Outline each uninfected red blood cell.
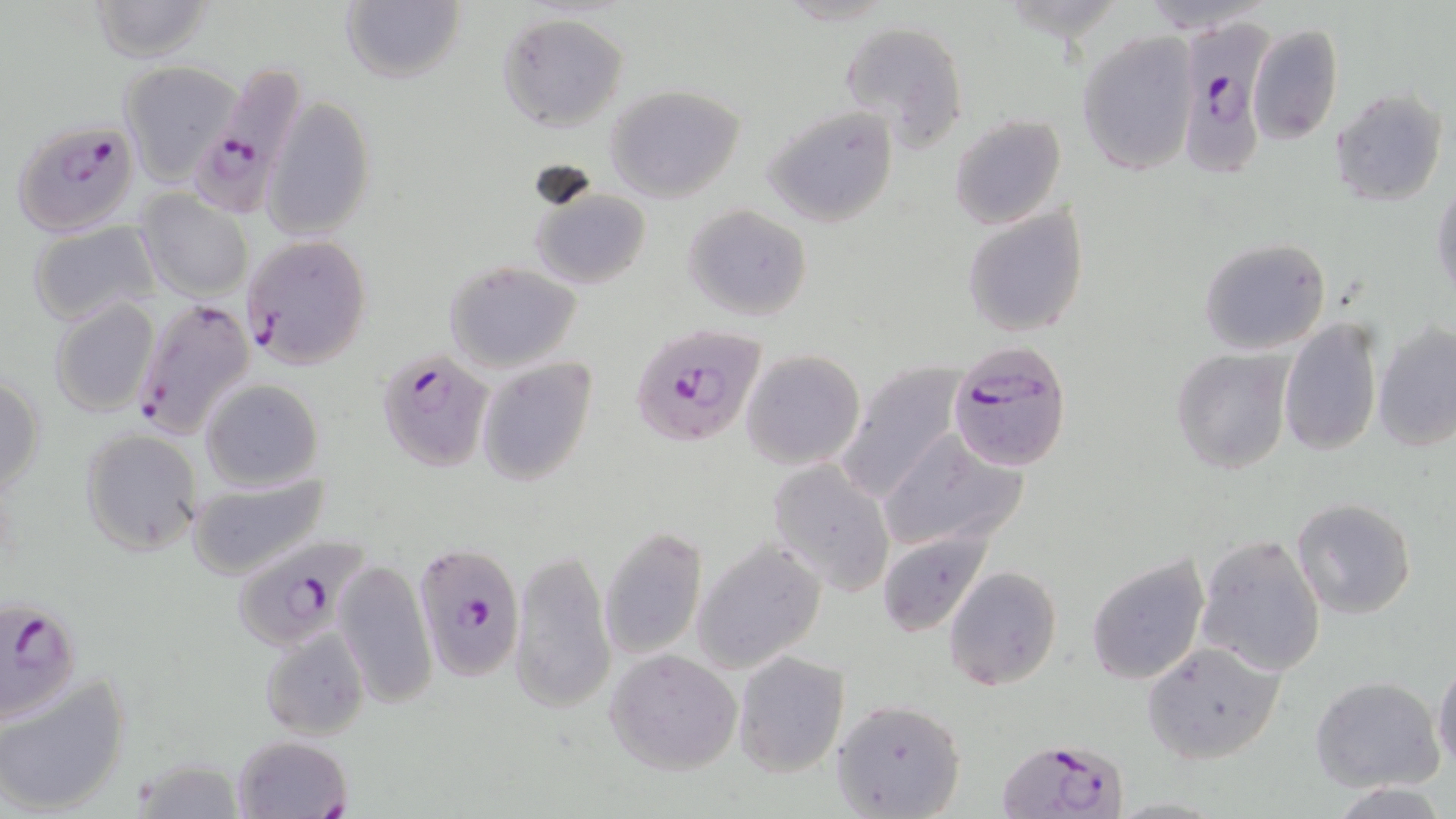
Approximate bounding boxes as (x1, y1, x2, y2) in pixels.
Uninfected red blood cells: (84, 0, 219, 63), (340, 0, 465, 86), (498, 12, 627, 131), (838, 19, 969, 152), (1249, 24, 1343, 144), (1076, 33, 1199, 174), (119, 62, 242, 186), (608, 85, 744, 202), (1331, 88, 1447, 207), (264, 99, 376, 239), (762, 105, 898, 227), (950, 114, 1066, 231), (1431, 175, 1456, 303), (530, 183, 651, 291), (134, 191, 253, 300), (682, 203, 813, 321), (962, 205, 1089, 338), (28, 222, 162, 329), (1198, 238, 1331, 356), (443, 258, 584, 373), (48, 298, 160, 419), (1277, 318, 1383, 458), (1373, 322, 1456, 453), (1171, 347, 1293, 475), (741, 348, 866, 470), (476, 357, 596, 487), (836, 359, 969, 507), (0, 374, 45, 495), (202, 379, 324, 489), (79, 428, 202, 554), (876, 431, 1029, 554), (768, 461, 896, 597), (185, 471, 335, 581), (1290, 497, 1418, 620), (599, 527, 705, 661), (877, 531, 992, 636), (1195, 533, 1327, 677), (691, 537, 827, 673), (511, 546, 614, 713), (1085, 553, 1211, 685), (333, 561, 436, 708), (944, 565, 1063, 691), (260, 624, 371, 740), (1142, 640, 1286, 764), (606, 648, 743, 775), (733, 651, 848, 776), (1432, 657, 1456, 773), (0, 671, 130, 819), (1310, 675, 1443, 791), (830, 699, 966, 818), (231, 734, 351, 818), (131, 759, 249, 817), (1334, 783, 1449, 818).

slide-level diagnosis = Plasmodium falciparum
modality = light microscopy
preparation = thin blood smear
stain = May-Grünwald-Giemsa
image size = 1456×819 pixels
magnification = 1000x
field of view = single
Plasmodium falciparum-infected red blood cell locations = approximate bounding boxes as (x1, y1, x2, y2) in pixels: (1174, 15, 1272, 184), (201, 63, 308, 211), (12, 118, 143, 236), (241, 233, 372, 369), (131, 298, 256, 436), (627, 323, 772, 448), (948, 343, 1074, 471), (375, 348, 493, 473), (230, 535, 371, 650), (414, 543, 525, 678), (2, 595, 85, 722), (991, 741, 1131, 819)